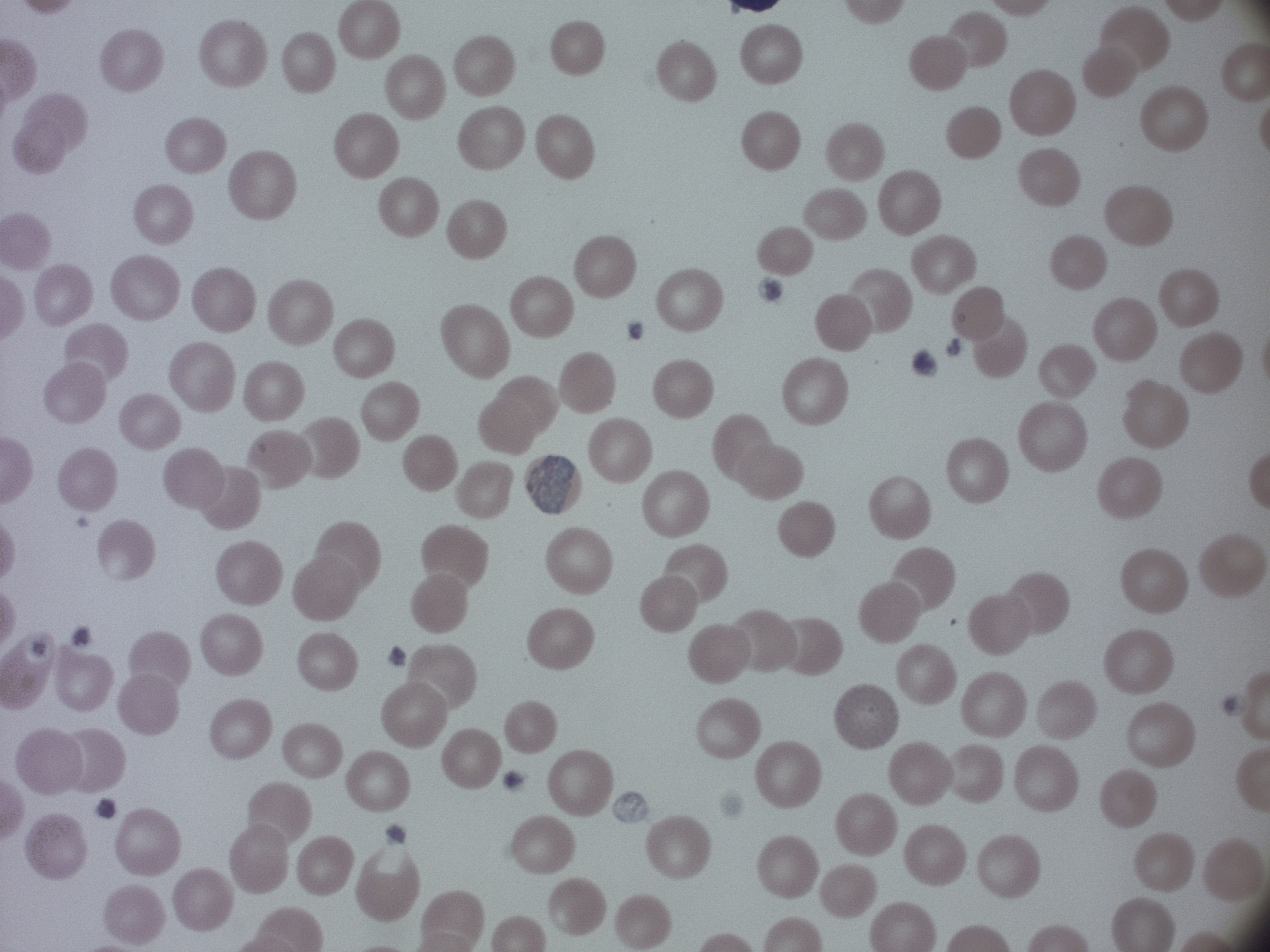

Approximate bounding boxes as (x1,y1)-(x2,y2) corner pairs in pixels, from the source annotation, which is not necessarily exhaustive.
Summary:
  - Gametocyte locations: (526,455)-(576,514)
  - Microscope: Leica DM2000 with built-in camera
  - Magnification: 100x
  - Image size: 1270×952 pixels
  - Field of view: single
  - Stain: Giemsa
  - Species: Plasmodium malariae
  - Preparation: thin blood film